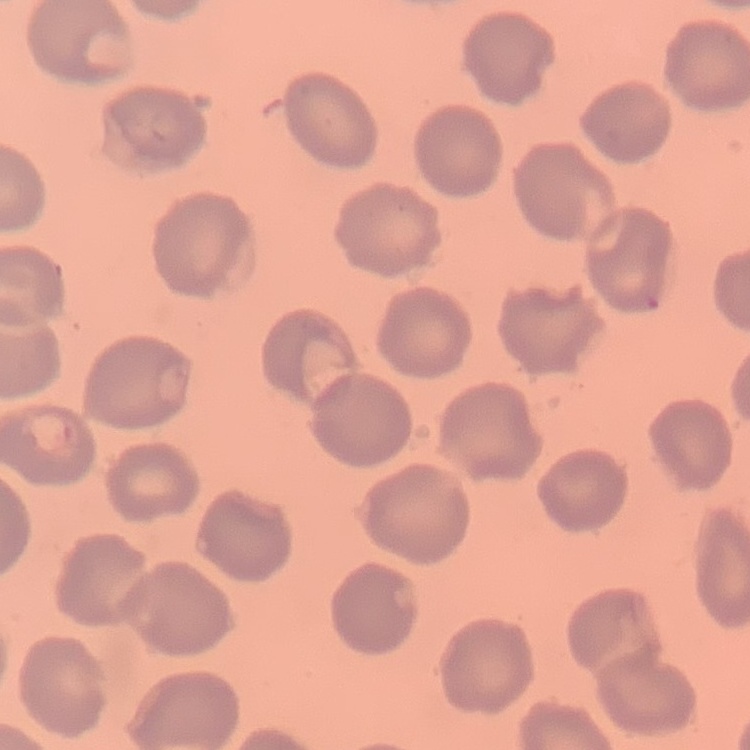

The red blood cells show no rouleaux formation. Thin blood smear. Stained with either Field's or Giemsa. Square crop of a larger photomicrograph.